Locate every white blood cell.
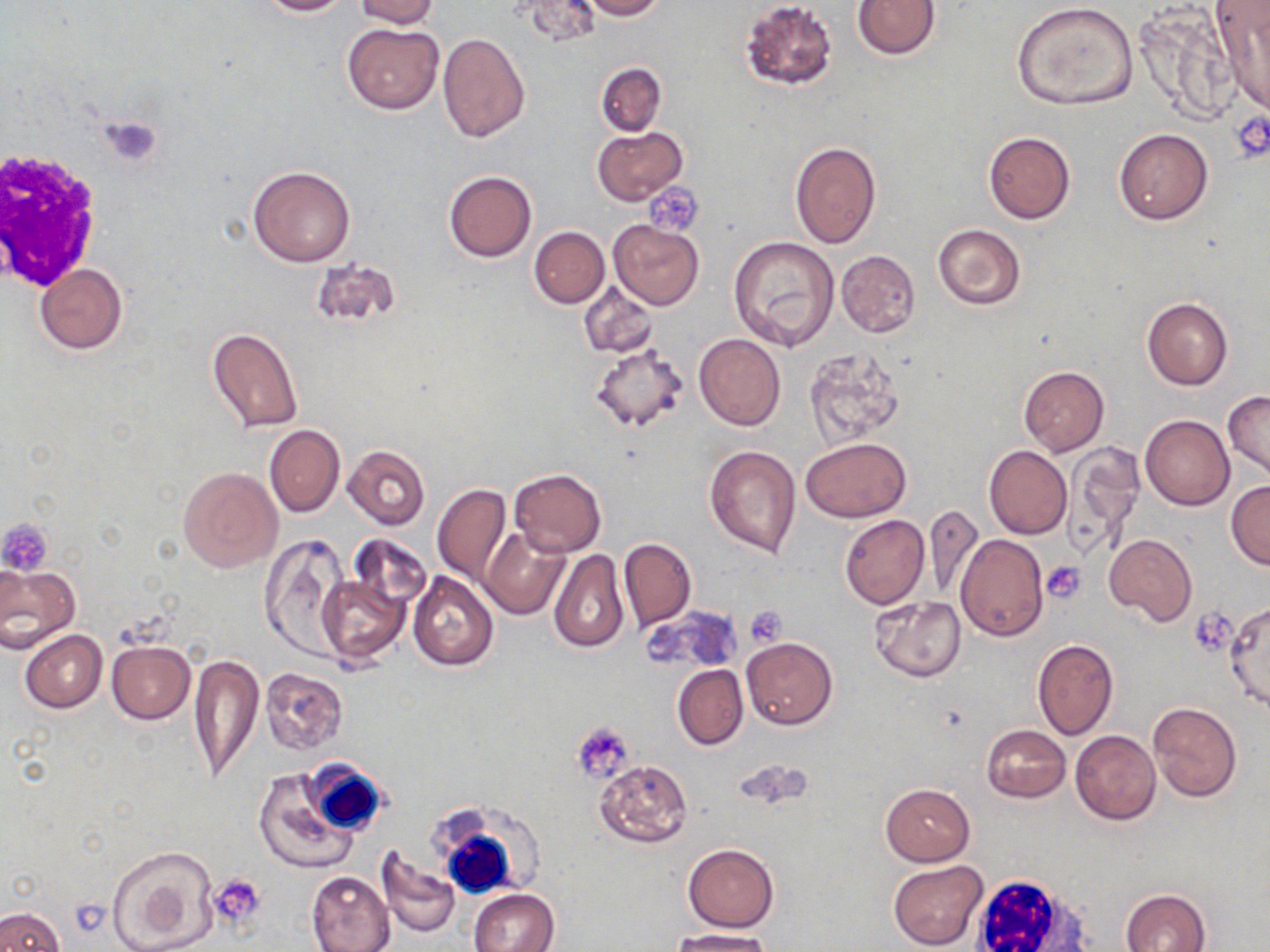

Approximate bounding boxes as named x1/y1/x2/y2 corners in pixels.
White blood cells: (x1=1, y1=149, x2=103, y2=289), (x1=298, y1=762, x2=389, y2=837), (x1=425, y1=803, x2=551, y2=895), (x1=971, y1=876, x2=1094, y2=952).

Summary:
  - Uninfected red blood cell locations: (x1=257, y1=0, x2=353, y2=17), (x1=353, y1=0, x2=441, y2=29), (x1=516, y1=0, x2=601, y2=47), (x1=580, y1=0, x2=666, y2=20), (x1=853, y1=0, x2=940, y2=59), (x1=738, y1=1, x2=839, y2=90), (x1=1011, y1=2, x2=1140, y2=111), (x1=1211, y1=2, x2=1270, y2=113), (x1=1138, y1=8, x2=1240, y2=125), (x1=341, y1=21, x2=443, y2=114), (x1=438, y1=33, x2=529, y2=142), (x1=596, y1=62, x2=666, y2=136), (x1=592, y1=127, x2=687, y2=205), (x1=1114, y1=128, x2=1213, y2=225), (x1=983, y1=131, x2=1076, y2=224), (x1=789, y1=141, x2=882, y2=249), (x1=248, y1=166, x2=356, y2=267), (x1=442, y1=171, x2=537, y2=262), (x1=609, y1=219, x2=704, y2=310), (x1=933, y1=223, x2=1027, y2=309), (x1=530, y1=227, x2=609, y2=307), (x1=729, y1=237, x2=841, y2=352), (x1=835, y1=249, x2=921, y2=338), (x1=311, y1=257, x2=403, y2=331), (x1=35, y1=264, x2=128, y2=354), (x1=579, y1=284, x2=658, y2=358), (x1=1142, y1=299, x2=1232, y2=390), (x1=207, y1=327, x2=303, y2=434), (x1=693, y1=334, x2=786, y2=432), (x1=590, y1=341, x2=690, y2=434), (x1=804, y1=349, x2=907, y2=447), (x1=1019, y1=367, x2=1109, y2=456), (x1=1223, y1=391, x2=1270, y2=484), (x1=1139, y1=415, x2=1234, y2=510), (x1=265, y1=425, x2=345, y2=518), (x1=800, y1=436, x2=912, y2=522), (x1=1063, y1=442, x2=1145, y2=555), (x1=704, y1=444, x2=801, y2=557), (x1=344, y1=445, x2=430, y2=530), (x1=985, y1=446, x2=1071, y2=539), (x1=356, y1=447, x2=475, y2=553), (x1=178, y1=467, x2=282, y2=571), (x1=509, y1=468, x2=606, y2=556), (x1=1226, y1=480, x2=1270, y2=570), (x1=432, y1=485, x2=511, y2=586), (x1=921, y1=504, x2=984, y2=602), (x1=840, y1=514, x2=930, y2=609), (x1=480, y1=525, x2=570, y2=619), (x1=1105, y1=533, x2=1196, y2=627), (x1=346, y1=534, x2=430, y2=619), (x1=956, y1=534, x2=1049, y2=641), (x1=259, y1=535, x2=351, y2=661), (x1=619, y1=537, x2=696, y2=630), (x1=549, y1=549, x2=629, y2=653), (x1=0, y1=564, x2=80, y2=650), (x1=408, y1=572, x2=499, y2=672), (x1=318, y1=573, x2=409, y2=665), (x1=869, y1=596, x2=965, y2=682), (x1=1225, y1=601, x2=1270, y2=712), (x1=647, y1=607, x2=742, y2=674), (x1=20, y1=630, x2=107, y2=713), (x1=742, y1=637, x2=837, y2=730), (x1=1033, y1=639, x2=1118, y2=739), (x1=106, y1=640, x2=194, y2=724), (x1=189, y1=653, x2=263, y2=784), (x1=672, y1=665, x2=747, y2=750), (x1=260, y1=667, x2=348, y2=754), (x1=1147, y1=702, x2=1243, y2=802), (x1=981, y1=725, x2=1070, y2=802), (x1=1070, y1=730, x2=1161, y2=825), (x1=594, y1=759, x2=693, y2=849), (x1=253, y1=769, x2=358, y2=873), (x1=880, y1=783, x2=975, y2=866), (x1=683, y1=844, x2=777, y2=931), (x1=106, y1=845, x2=219, y2=952), (x1=376, y1=846, x2=460, y2=938), (x1=887, y1=860, x2=987, y2=949), (x1=307, y1=870, x2=396, y2=952), (x1=470, y1=889, x2=559, y2=952), (x1=1120, y1=889, x2=1210, y2=952), (x1=0, y1=906, x2=67, y2=952), (x1=669, y1=928, x2=775, y2=952)
  - Platelet locations: (x1=1231, y1=112, x2=1270, y2=162), (x1=98, y1=114, x2=164, y2=169), (x1=642, y1=183, x2=703, y2=237), (x1=0, y1=518, x2=54, y2=575), (x1=1041, y1=561, x2=1085, y2=603), (x1=745, y1=607, x2=788, y2=646), (x1=1189, y1=610, x2=1234, y2=653), (x1=573, y1=721, x2=636, y2=782), (x1=208, y1=875, x2=266, y2=931)
  - Slide-level diagnosis: negative for blood parasites
  - Stain: May-Grünwald-Giemsa
  - Image size: 1270×952 pixels
  - Modality: optical microscopy
  - Preparation: thin blood film
  - Magnification: 1000x
  - Field of view: one of a larger specimen